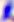
{
  "magnification": "400x",
  "modality": "micrograph",
  "identification": "Toxoplasma gondii"
}